Give the extent of all Plasmodium malariae-infected red blood cells.
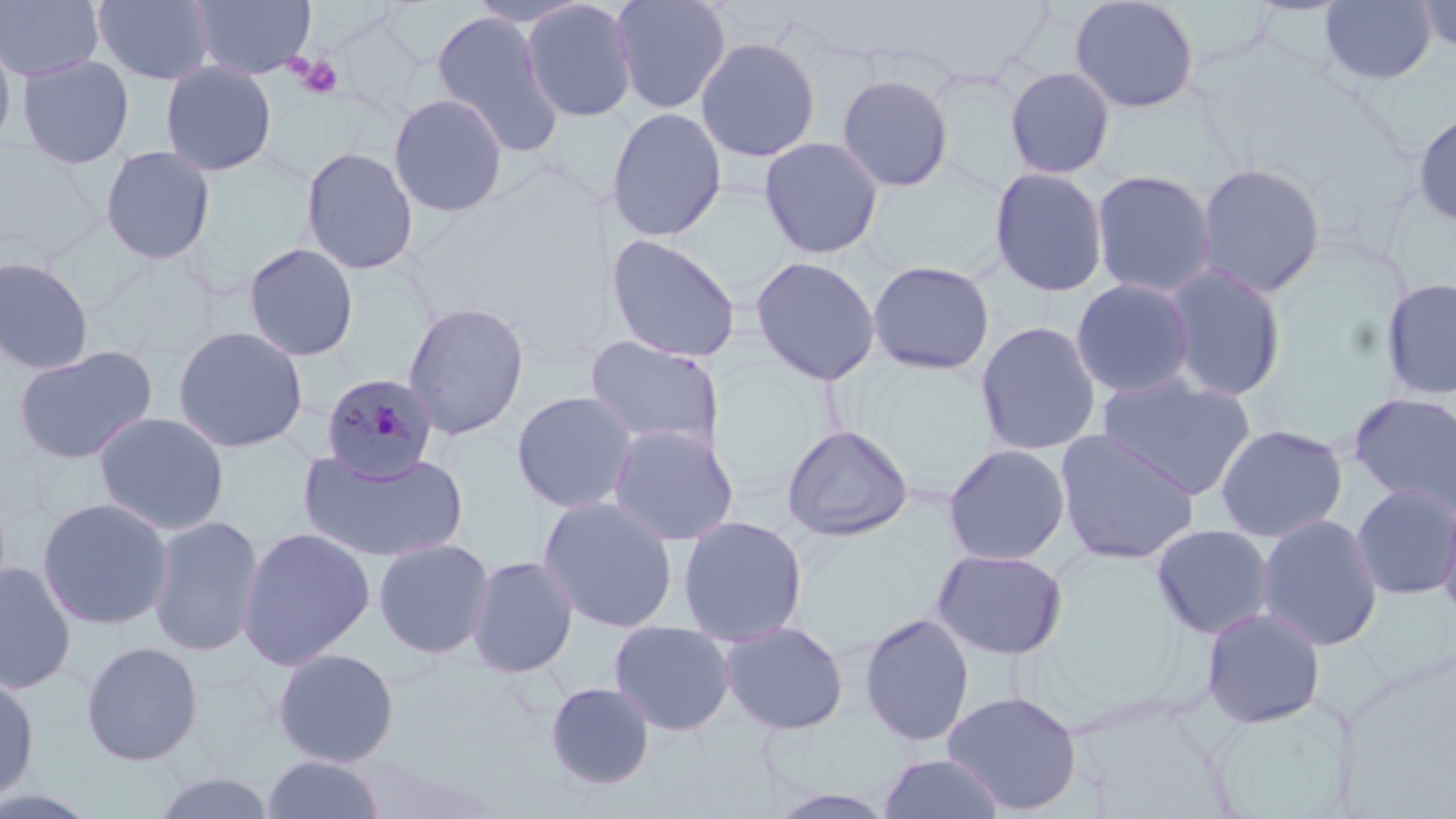

Approximate bounding boxes as [x1, y1, x2, y2] in pixels.
Plasmodium malariae-infected red blood cells: [320, 372, 439, 483].

Uninfected red blood cell locations: [92, 0, 216, 86], [188, 0, 316, 80], [610, 0, 732, 115], [1069, 0, 1200, 114], [1319, 0, 1436, 85], [0, 1, 105, 82], [519, 1, 639, 123], [1414, 1, 1456, 55], [430, 9, 565, 158], [0, 32, 17, 156], [696, 36, 821, 163], [16, 54, 135, 169], [156, 61, 276, 178], [1004, 66, 1116, 179], [836, 73, 955, 192], [388, 92, 508, 218], [606, 107, 727, 242], [1412, 109, 1456, 229], [758, 136, 884, 259], [100, 145, 216, 266], [300, 146, 419, 275], [1194, 161, 1327, 300], [989, 166, 1109, 297], [1090, 169, 1216, 298], [604, 233, 742, 363], [242, 242, 360, 362], [749, 255, 881, 386], [0, 256, 95, 374], [867, 260, 995, 376], [1160, 263, 1288, 402], [1379, 275, 1456, 401], [1070, 278, 1197, 399], [403, 301, 530, 440], [974, 321, 1102, 456], [171, 325, 309, 453], [583, 334, 725, 456], [12, 344, 159, 466], [1096, 371, 1256, 500], [511, 390, 639, 513], [1347, 392, 1456, 517], [92, 411, 230, 536], [780, 423, 913, 542], [1215, 423, 1348, 542], [607, 424, 740, 546], [1054, 429, 1201, 565], [942, 443, 1072, 565], [297, 446, 470, 563], [1350, 484, 1456, 600], [1436, 492, 1456, 627], [537, 495, 680, 634], [36, 496, 174, 631], [147, 514, 264, 658], [677, 514, 809, 647], [1255, 514, 1384, 651], [1150, 524, 1275, 640], [236, 526, 376, 671], [372, 537, 495, 659], [931, 548, 1068, 660], [466, 554, 578, 678], [0, 560, 77, 695], [1201, 606, 1327, 729], [859, 612, 975, 748], [609, 619, 737, 736], [718, 620, 849, 735], [80, 640, 204, 765], [271, 647, 400, 766], [0, 673, 40, 806], [545, 681, 656, 791], [942, 689, 1083, 815], [878, 752, 1005, 819], [261, 754, 386, 819], [146, 771, 281, 818], [0, 785, 104, 818], [765, 788, 899, 818]. Platelet locations: [292, 54, 343, 99]. Slide-level diagnosis: Plasmodium malariae. 1000x magnification. Image is 1456×819 pixels. Single field of view. May-Grünwald-Giemsa-stained preparation. Light microscopy. Thin blood smear.